Classify this cell by malaria status.
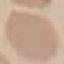

It is uninfected.

Giemsa stain. Cell patch, automatically extracted from a larger field of view and resized to 64 × 64 pixels. Acquired by smartphone through the microscope eyepiece. Thin blood film.